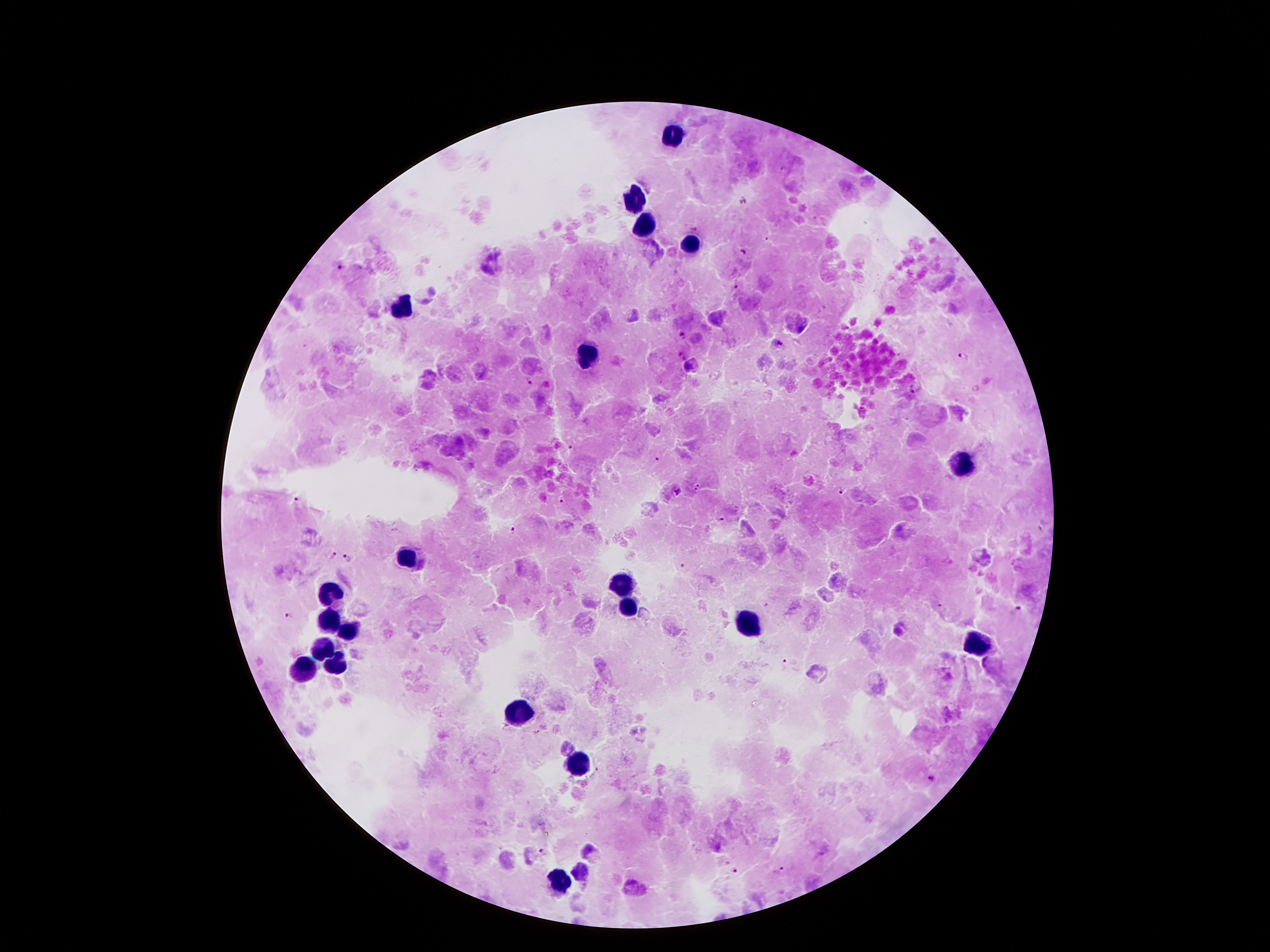

Approximate centers as (x, y) in pixels.
Summary:
  - Leukocyte locations: (669, 133), (635, 200), (645, 223), (691, 245), (402, 308), (589, 357), (962, 463), (409, 558), (622, 583), (333, 590), (630, 611), (331, 622), (747, 626), (352, 629), (975, 646), (324, 648), (337, 667), (305, 672), (514, 715), (577, 762), (561, 883)
  - Malaria parasite locations: (742, 200), (695, 229), (741, 251), (339, 268), (735, 284), (682, 335), (777, 345), (963, 356), (687, 366), (531, 382), (916, 387), (572, 447), (656, 458), (695, 484), (842, 493), (561, 499), (297, 500), (720, 518), (513, 529), (332, 556), (349, 556), (684, 566), (941, 608), (1017, 608), (289, 615), (785, 663), (932, 779), (542, 852), (783, 868), (736, 871)
  - Magnification: 100x
  - Patient malaria status: positive for Plasmodium falciparum
  - Image size: 1270×952 pixels
  - Preparation: thick blood smear
  - Capture: smartphone through the microscope eyepiece
  - Stain: Giemsa
  - Field of view: one from this slide